Report the malaria status of this cell.
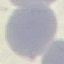
It is uninfected.

capture = smartphone camera at the microscope eyepiece
image type = automatically extracted cell patch, resized to 64 × 64 pixels
stain = Giemsa
preparation = thin blood film